Give the extent of all Trypanosoma brucei.
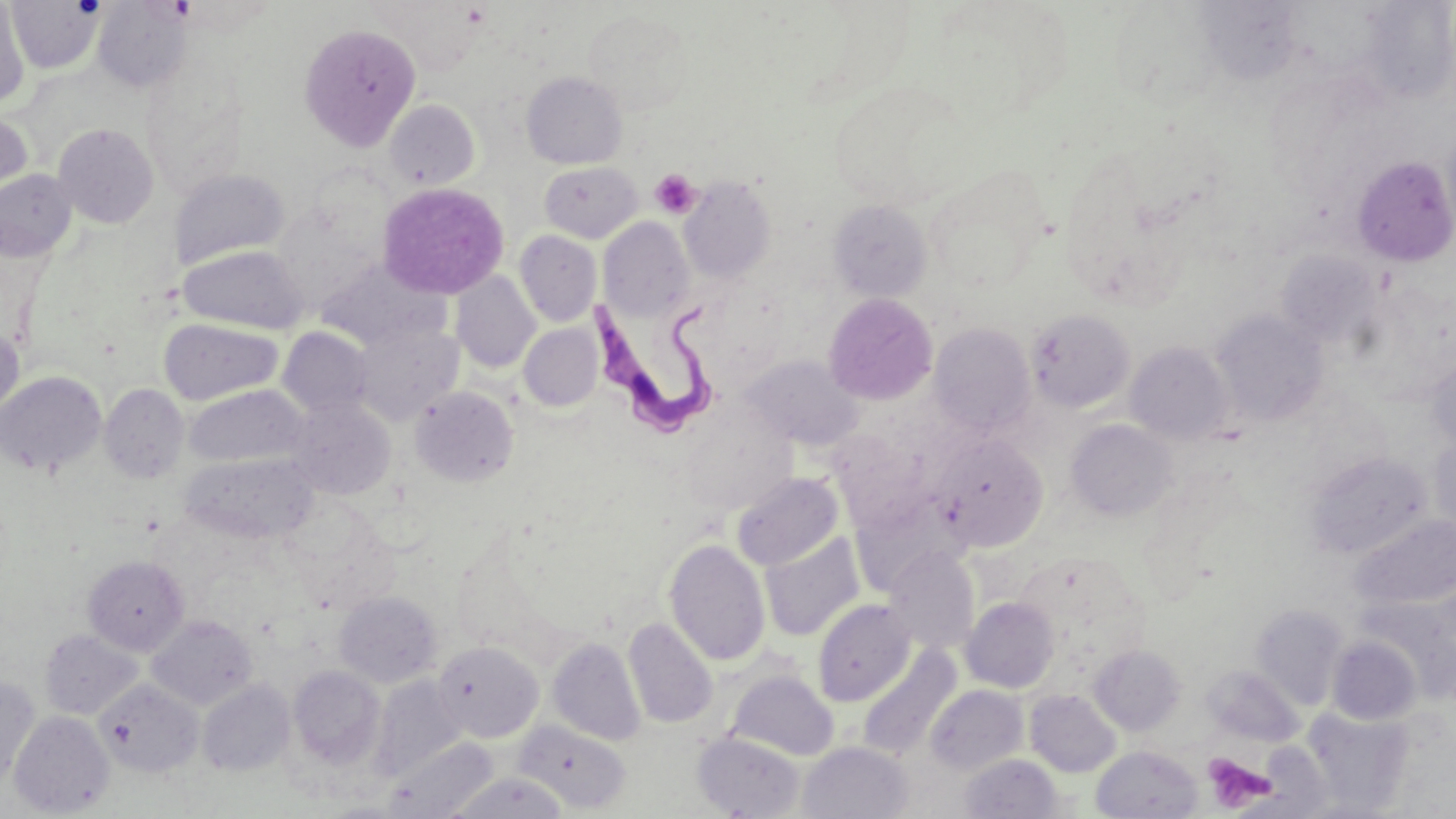
Approximate bounding boxes as (x1,y1)-(x2,y2) corner pairs in pixels.
Trypanosoma brucei: (591,294)-(725,438).

Summary:
  - Platelet locations: (649,168)-(701,219), (1202,752)-(1276,814)
  - Uninfected red blood cell locations: (6,1)-(103,74), (92,1)-(193,92), (369,1)-(486,73), (0,2)-(31,107), (1109,3)-(1214,109), (582,8)-(695,116), (299,22)-(421,150), (521,71)-(628,169), (828,81)-(972,209), (385,99)-(481,190), (0,109)-(32,212), (52,123)-(159,229), (1352,156)-(1456,267), (539,162)-(642,242), (0,168)-(77,262), (169,168)-(290,269), (928,173)-(1045,291), (679,176)-(776,282), (375,182)-(509,300), (827,199)-(932,302), (273,204)-(381,306), (598,217)-(695,321), (514,230)-(602,326), (178,244)-(307,334), (1276,251)-(1382,349), (451,271)-(540,373), (823,293)-(938,405), (1026,309)-(1135,413), (1211,309)-(1328,427), (159,318)-(283,405), (928,322)-(1036,437), (0,323)-(24,420), (353,323)-(464,425), (519,324)-(603,411), (277,327)-(374,419), (1125,342)-(1233,446), (1426,353)-(1456,453), (743,356)-(862,450), (0,371)-(106,476), (99,384)-(189,483), (185,385)-(305,468), (410,386)-(519,487), (287,397)-(396,499), (681,410)-(798,515), (1066,419)-(1178,521), (934,435)-(1047,549), (1429,435)-(1456,536), (1305,450)-(1433,559), (182,452)-(317,545), (732,472)-(843,570), (1350,514)-(1456,611), (760,535)-(863,641), (664,538)-(770,666), (884,546)-(980,653), (82,555)-(189,655), (334,591)-(442,687), (960,597)-(1059,693), (813,599)-(915,705), (1251,603)-(1349,710), (147,615)-(257,710), (623,617)-(717,729), (39,629)-(143,719), (1327,636)-(1422,725), (548,637)-(645,745), (432,641)-(543,742), (1089,645)-(1185,735), (856,646)-(960,761), (1203,665)-(1304,746), (288,666)-(386,771), (728,669)-(838,760), (0,675)-(40,789), (371,675)-(466,779), (97,679)-(203,777), (197,679)-(295,776), (925,684)-(1028,774), (1025,689)-(1121,777), (1304,709)-(1416,814), (8,710)-(115,817), (513,720)-(630,813), (693,732)-(805,818), (386,737)-(496,818), (798,741)-(914,819), (1091,746)-(1203,819), (960,753)-(1063,818), (447,772)-(569,818)
  - Slide-level diagnosis: Trypanosoma brucei
  - Magnification: 1000x
  - Field of view: one of a larger specimen
  - Preparation: thin blood film
  - Image size: 1456×819 pixels
  - Stain: May-Grünwald-Giemsa
  - Modality: optical microscopy